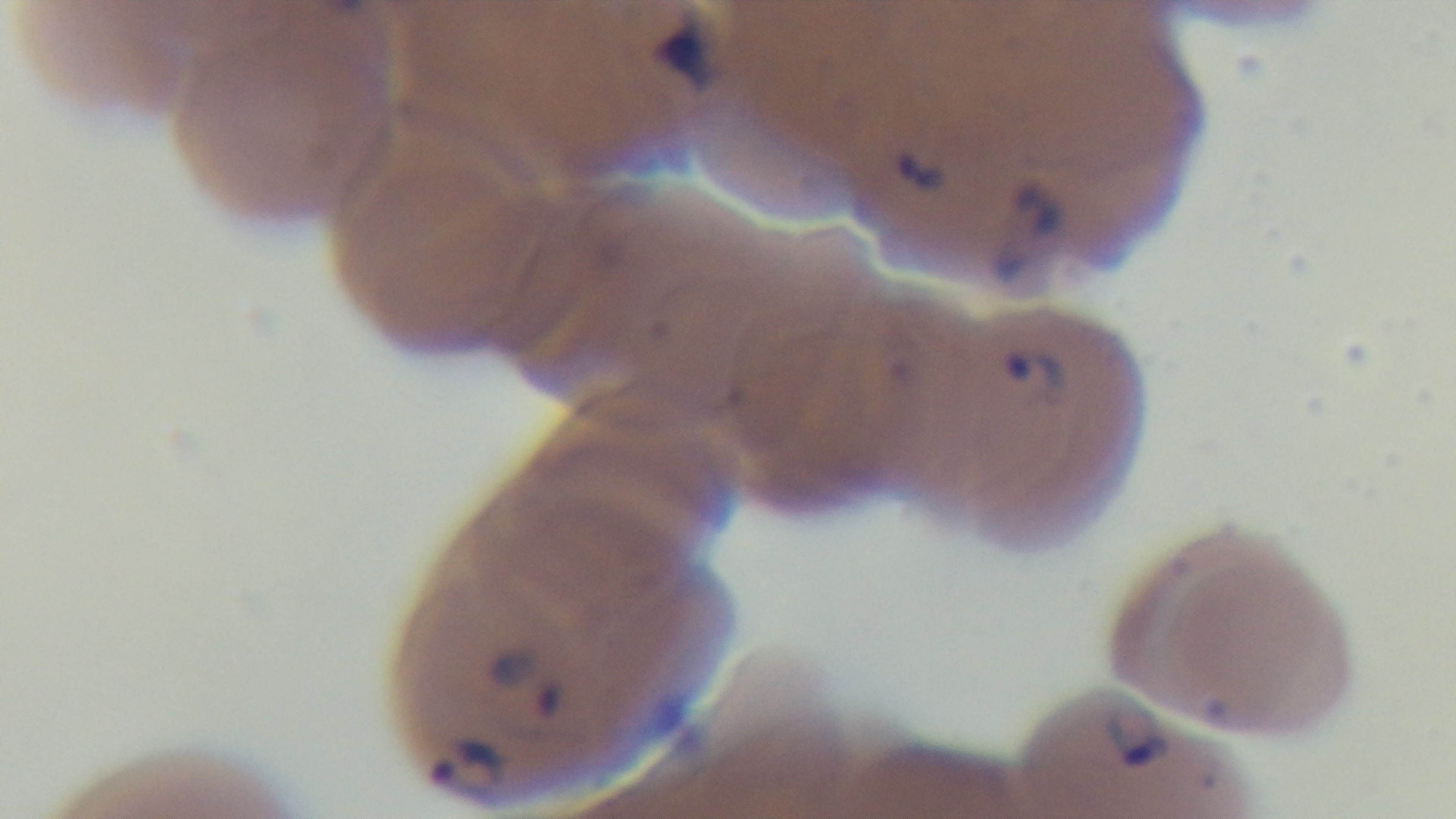
Summary:
  - Modality: light microscopy
  - Preparation: thin
  - Capture: mounted 4K digital camera
  - Malaria status: infected
  - Stain: Giemsa
  - Objective: 100x oil immersion
  - Field of view: one from the slide